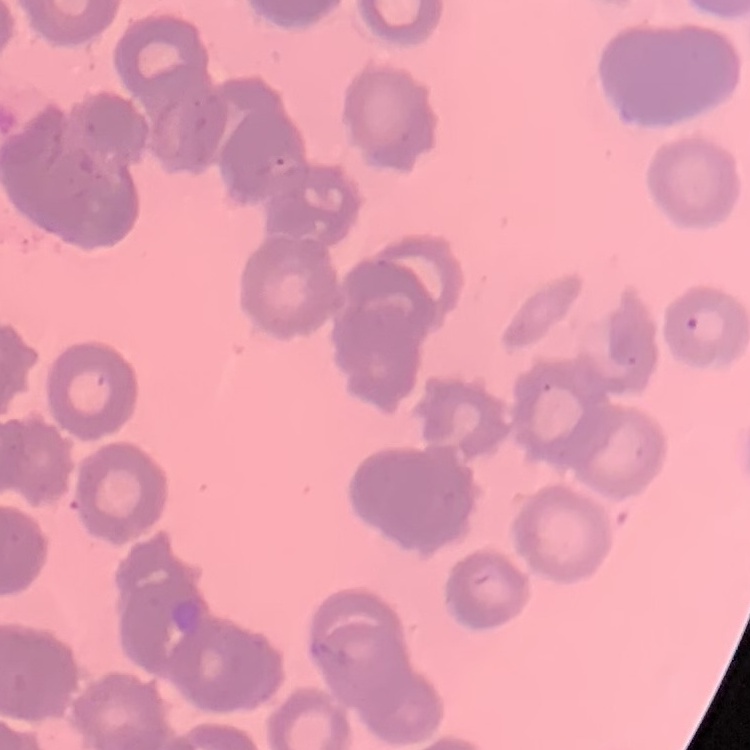

Summary:
  - Erythrocyte morphology: rouleaux formation
  - Stain: Field's or Giemsa
  - Preparation: thin blood film
  - Image type: one tile cut from a larger photomicrograph